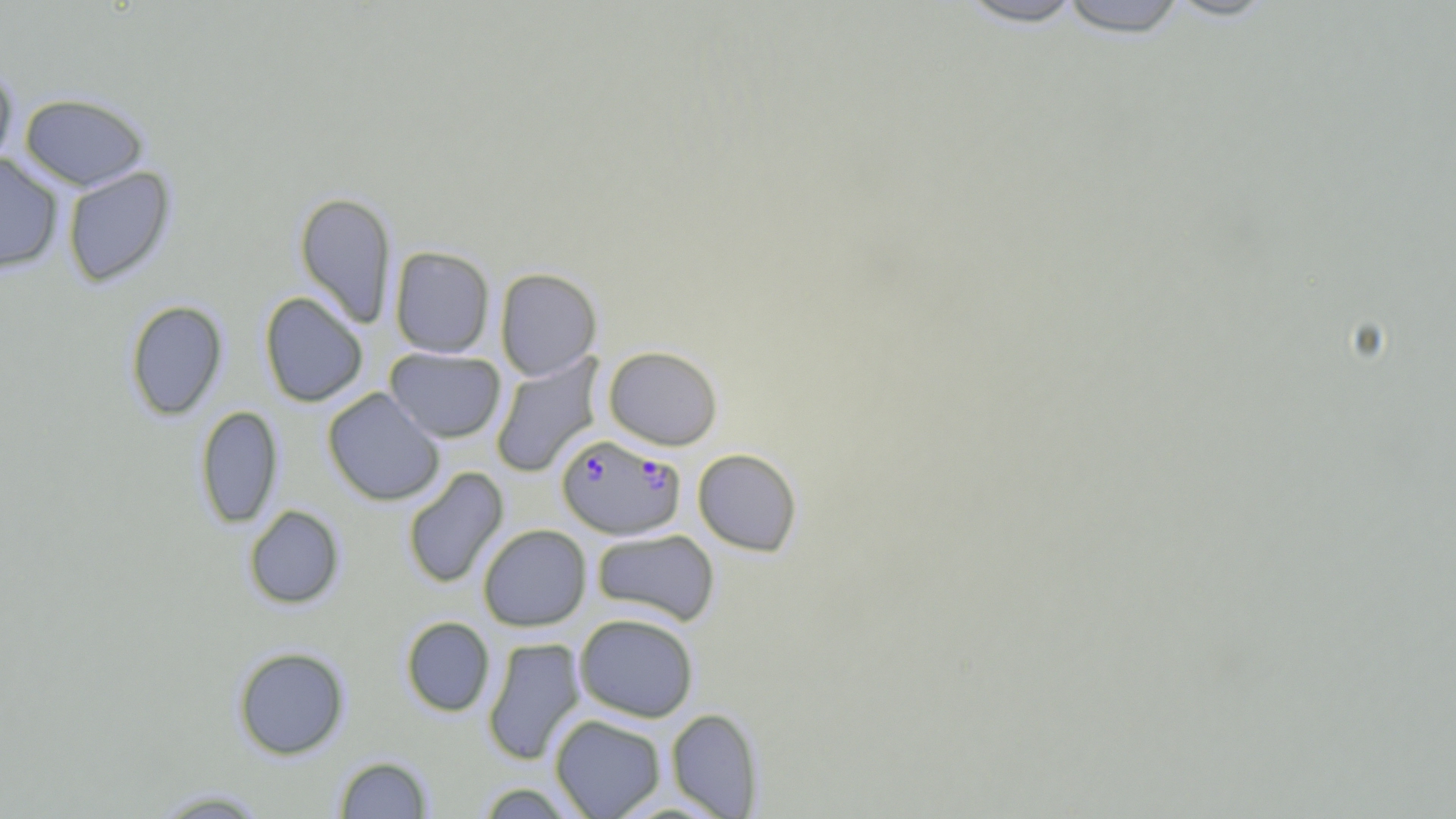 Approximate bounding boxes as named x1/y1/x2/y2 corners in pixels. Plasmodium falciparum-infected red blood cell locations: (x1=556, y1=434, x2=685, y2=540). Uninfected red blood cell locations: (x1=952, y1=0, x2=1090, y2=29), (x1=1055, y1=0, x2=1192, y2=38), (x1=0, y1=64, x2=18, y2=173), (x1=19, y1=93, x2=150, y2=190), (x1=0, y1=154, x2=64, y2=273), (x1=62, y1=166, x2=177, y2=287), (x1=294, y1=191, x2=397, y2=328), (x1=389, y1=246, x2=495, y2=358), (x1=494, y1=267, x2=602, y2=381), (x1=258, y1=291, x2=369, y2=407), (x1=124, y1=300, x2=228, y2=421), (x1=603, y1=345, x2=723, y2=450), (x1=385, y1=348, x2=506, y2=443), (x1=490, y1=354, x2=605, y2=478), (x1=322, y1=387, x2=445, y2=506), (x1=195, y1=405, x2=283, y2=528), (x1=692, y1=448, x2=802, y2=556), (x1=402, y1=466, x2=509, y2=589), (x1=243, y1=505, x2=345, y2=609), (x1=478, y1=524, x2=591, y2=631), (x1=592, y1=529, x2=720, y2=625), (x1=574, y1=613, x2=699, y2=722), (x1=400, y1=616, x2=495, y2=717), (x1=482, y1=637, x2=586, y2=765), (x1=232, y1=646, x2=350, y2=760), (x1=666, y1=708, x2=764, y2=818), (x1=549, y1=714, x2=666, y2=818), (x1=333, y1=755, x2=434, y2=818), (x1=475, y1=781, x2=581, y2=818), (x1=149, y1=788, x2=273, y2=818). Slide-level diagnosis: Plasmodium falciparum. Thin blood smear. Image is 1456×819 pixels. Single field of view. May-Grünwald-Giemsa-stained preparation. Light microscopy. 1000x magnification.